Report the malaria status of this cell.
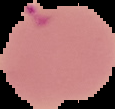

It is parasitized.

preparation: thin blood film
image_size: 115×109 pixels
image_type: segmented cell region on a black background